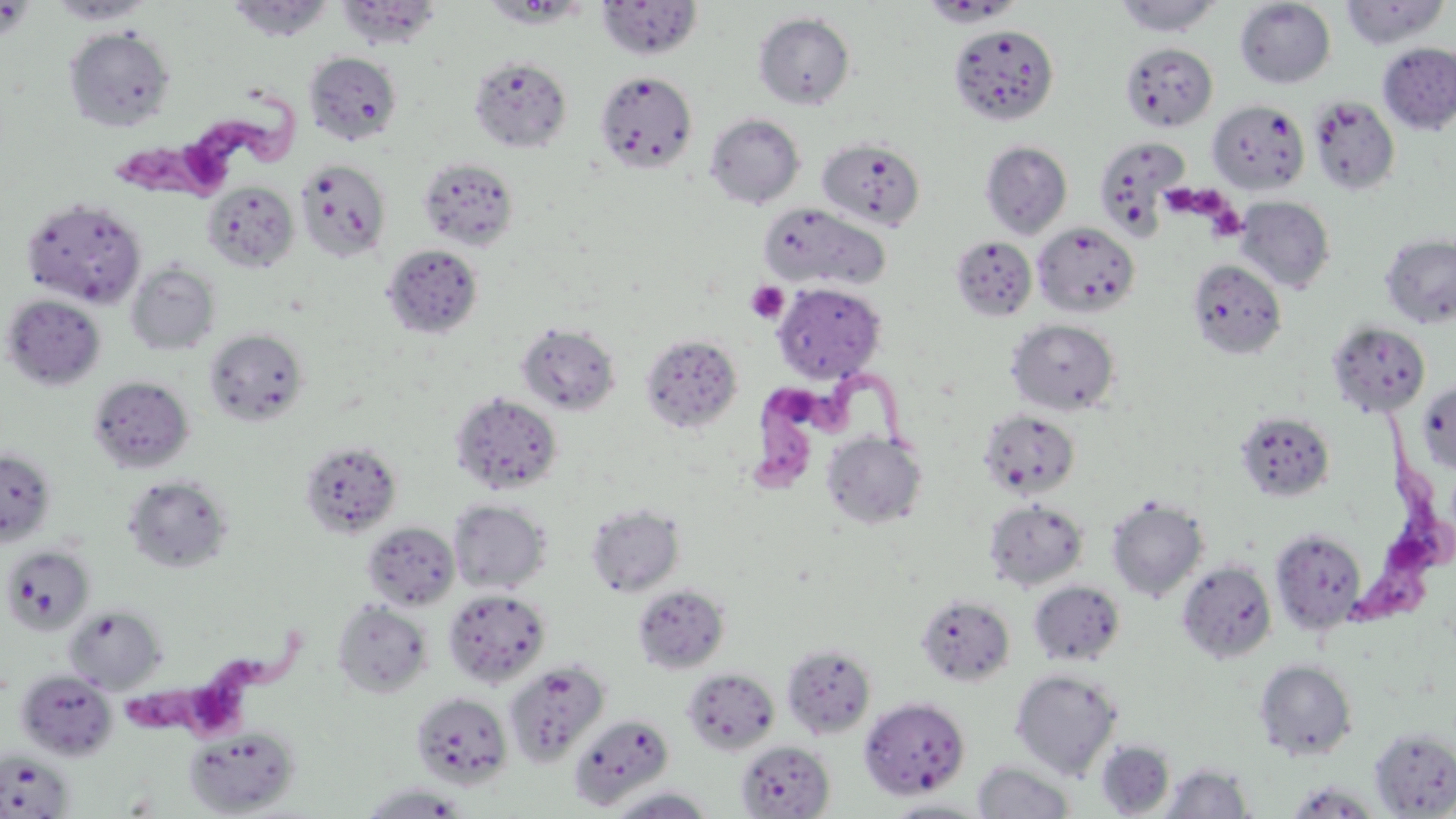

Summary:
  - Coordinate format: approximate bounding boxes as [x1, y1, x2, y2] in pixels
  - Platelet locations: [1165, 185, 1213, 215], [1207, 196, 1248, 241], [746, 281, 789, 324]
  - Trypanosoma brucei locations: [111, 92, 302, 199], [747, 361, 924, 503], [1337, 400, 1449, 636], [111, 639, 308, 741]
  - Uninfected red blood cell locations: [47, 0, 155, 25], [226, 0, 334, 42], [480, 0, 592, 28], [597, 0, 703, 60], [1113, 0, 1223, 37], [1235, 0, 1336, 88], [1339, 0, 1451, 49], [335, 1, 442, 49], [753, 12, 856, 109], [948, 24, 1060, 126], [63, 26, 176, 132], [1120, 41, 1218, 131], [1377, 42, 1456, 135], [303, 51, 403, 145], [469, 56, 572, 153], [595, 70, 698, 174], [1308, 94, 1401, 196], [1207, 99, 1310, 195], [704, 113, 805, 208], [1092, 135, 1190, 238], [816, 137, 926, 231], [980, 141, 1073, 239], [417, 157, 519, 252], [295, 159, 392, 262], [201, 180, 299, 273], [1234, 196, 1335, 293], [20, 197, 148, 309], [757, 201, 890, 293], [1032, 221, 1140, 318], [1380, 233, 1456, 329], [949, 236, 1037, 322], [381, 243, 484, 339], [1187, 259, 1287, 360], [126, 261, 220, 356], [772, 282, 886, 382], [1, 294, 106, 391], [1006, 318, 1121, 416], [1327, 321, 1431, 417], [516, 322, 621, 416], [203, 328, 310, 427], [640, 333, 743, 434], [88, 376, 194, 474], [1417, 379, 1456, 475], [450, 392, 563, 495], [978, 409, 1081, 499], [1234, 410, 1336, 503], [822, 432, 927, 530], [299, 439, 403, 538], [0, 448, 58, 546], [122, 474, 233, 574], [1106, 495, 1209, 602], [448, 499, 551, 594], [983, 499, 1090, 591], [585, 502, 686, 597], [362, 521, 460, 611], [1270, 528, 1368, 635], [1, 545, 95, 636], [1176, 560, 1278, 664], [1027, 580, 1126, 668], [632, 584, 730, 674], [443, 587, 551, 688], [916, 594, 1016, 688], [332, 599, 434, 699], [63, 605, 167, 693], [781, 642, 877, 737], [1254, 659, 1358, 760], [503, 661, 609, 766], [682, 667, 780, 755], [1009, 668, 1123, 779], [15, 669, 118, 761], [410, 691, 514, 789], [859, 696, 970, 800], [569, 713, 674, 810], [183, 725, 301, 817], [1369, 727, 1456, 817], [736, 739, 835, 818], [1096, 740, 1175, 816], [0, 749, 76, 818], [972, 760, 1077, 818], [1159, 763, 1254, 819], [1283, 782, 1386, 818], [357, 783, 474, 818], [604, 786, 718, 818], [880, 798, 994, 818]
  - Slide-level diagnosis: Trypanosoma brucei
  - Preparation: thin blood smear
  - Magnification: 1000x
  - Modality: optical microscopy
  - Image size: 1456×819 pixels
  - Field of view: single
  - Stain: May-Grünwald-Giemsa